Describe the morphology of the red blood cells.
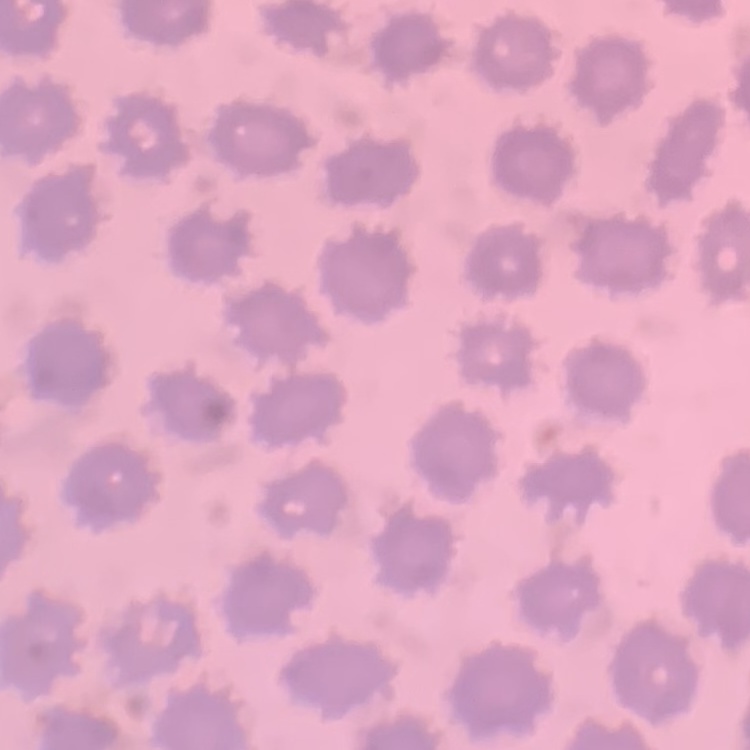

No rouleaux formation.

Summary:
  - Preparation: thin peripheral smear
  - Image type: one tile cut from a larger photomicrograph
  - Stain: Field's or Giemsa